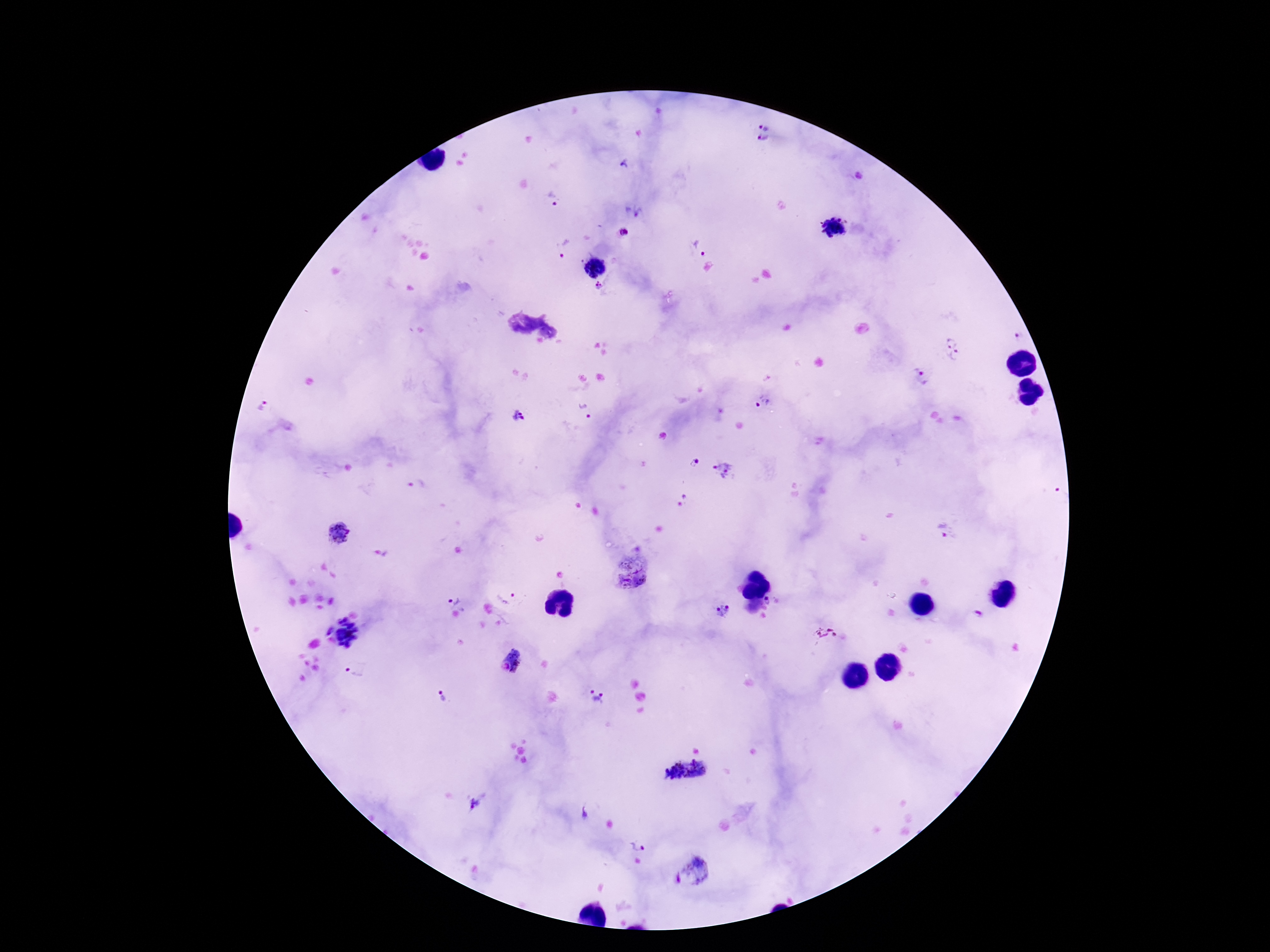
Approximate centers as {x, y} in pixels.
Summary:
  - Plasmodium parasite locations: {764, 126}, {764, 140}, {624, 164}, {550, 201}, {634, 212}, {833, 228}, {623, 232}, {703, 248}, {562, 256}, {593, 265}, {598, 286}, {1019, 337}, {955, 348}, {922, 375}, {761, 403}, {263, 407}, {585, 411}, {520, 416}, {694, 461}, {723, 468}, {416, 483}, {1062, 492}, {685, 496}, {943, 530}, {339, 532}, {632, 572}, {510, 599}, {769, 600}, {462, 601}, {722, 611}, {975, 615}, {351, 632}, {826, 633}, {357, 671}, {441, 692}, {598, 695}, {699, 770}, {673, 771}, {477, 804}, {584, 812}, {640, 844}, {704, 866}
  - Image size: 1270×952 pixels
  - Capture: smartphone camera through the microscope eyepiece
  - Field of view: one from this slide
  - Preparation: thick blood film
  - Magnification: 100x
  - Patient malaria status: infected
  - Stain: Giemsa